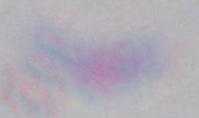
Summary:
  - Magnification: 1000x
  - Identification: Toxoplasma gondii
  - Modality: photomicrograph